Classify this cell by malaria status.
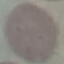
It is uninfected.

Summary:
  - Stain: Giemsa
  - Capture: smartphone through the microscope eyepiece
  - Preparation: thin blood smear
  - Image type: automatically extracted cell patch, resized to 64 × 64 pixels